Assess this cell for malaria.
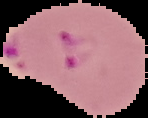
Parasitized.

From a thin blood smear. Image is 148×118 pixels. The area outside the segmented cell region is set to black.